Locate the red blood cells and classify each one as Plasmodium falciparum-infected, uninfected, or of indeterminate infection status.
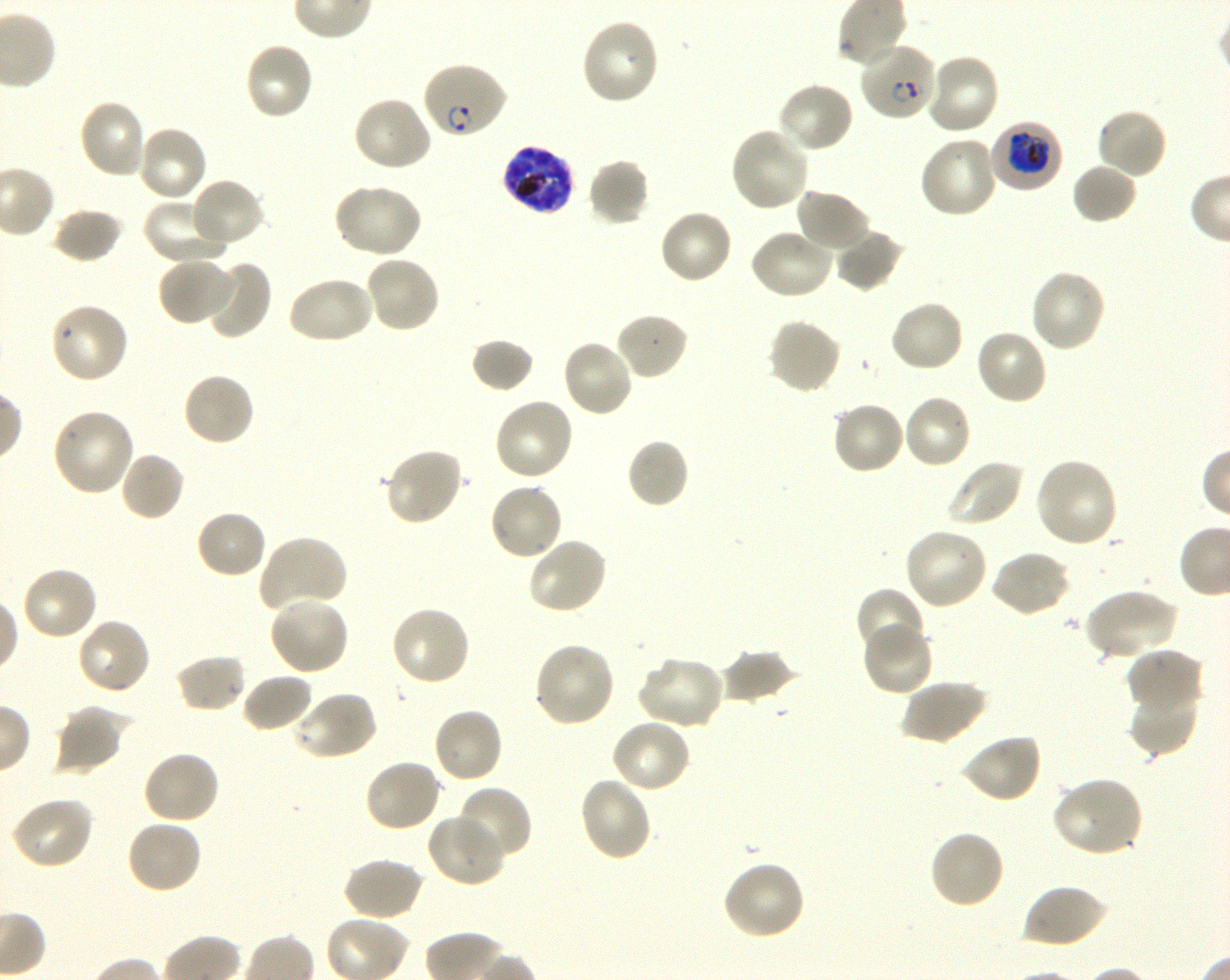
Approximate bounding boxes as (x1, y1, x2, y2) in pixels. Not every red blood cell is marked. A life-cycle stage — or a range of stages, where the recorded stages span more than one — follows each staged infected red blood cell.
Infected red blood cells: (860, 42, 937, 122) ring; (421, 61, 509, 141) ring; (990, 121, 1062, 192) trophozoite; (500, 144, 576, 215) schizont.
Uninfected red blood cells: (581, 18, 661, 106), (244, 42, 315, 122), (922, 52, 1001, 136), (776, 82, 855, 155), (352, 95, 434, 173), (77, 98, 149, 180), (1095, 106, 1168, 180), (135, 124, 210, 202), (729, 126, 811, 213), (917, 135, 998, 220), (587, 157, 651, 227), (1071, 162, 1138, 225), (188, 177, 266, 249), (333, 182, 422, 258), (794, 187, 872, 253), (141, 197, 230, 266), (51, 207, 124, 264), (658, 209, 733, 285), (748, 228, 834, 301), (834, 228, 906, 293), (364, 254, 442, 335), (156, 257, 236, 327), (202, 260, 270, 338), (1029, 268, 1107, 353), (286, 275, 375, 346), (888, 299, 964, 374), (49, 301, 130, 385), (614, 313, 689, 380), (766, 318, 843, 395), (975, 329, 1049, 406), (470, 337, 535, 393), (560, 338, 635, 418), (181, 371, 257, 447), (901, 393, 973, 470), (493, 397, 575, 482), (830, 400, 906, 475), (50, 407, 135, 498), (625, 438, 690, 510), (383, 446, 464, 528), (119, 451, 185, 522), (1032, 457, 1120, 549), (944, 458, 1024, 528), (487, 482, 564, 562), (194, 508, 268, 580), (902, 527, 989, 611), (257, 534, 349, 613), (527, 536, 609, 616), (989, 549, 1071, 617), (20, 566, 99, 642), (855, 587, 927, 661), (1083, 587, 1179, 661), (267, 595, 350, 676), (389, 604, 471, 688), (76, 617, 152, 696), (861, 623, 934, 698), (533, 641, 616, 729), (1126, 647, 1203, 713), (717, 648, 798, 705), (174, 654, 247, 714), (636, 655, 725, 730), (240, 672, 314, 733), (901, 679, 986, 746), (1128, 683, 1200, 756), (291, 690, 379, 762), (52, 704, 131, 777), (431, 706, 504, 785), (609, 718, 691, 794), (960, 733, 1043, 804), (142, 750, 221, 825), (363, 758, 443, 833), (578, 776, 653, 862), (1051, 776, 1144, 858), (456, 786, 533, 864), (10, 796, 95, 870), (425, 813, 505, 887), (126, 819, 202, 895), (928, 828, 1005, 909), (342, 858, 425, 921), (720, 860, 807, 942), (1021, 882, 1108, 949).
No red blood cells of indeterminate infection status observed.

donor blood group = O+
life-cycle stages observed = ring, trophozoite, schizont
preparation = thin blood film
culture = shaking in-vitro Plasmodium falciparum strain 3D7
field of view = single
stain = Giemsa
image size = 1230×980 pixels
objective = 100x, oil immersion, numerical aperture 1.30